Give the extent of all uninfected red blood cells.
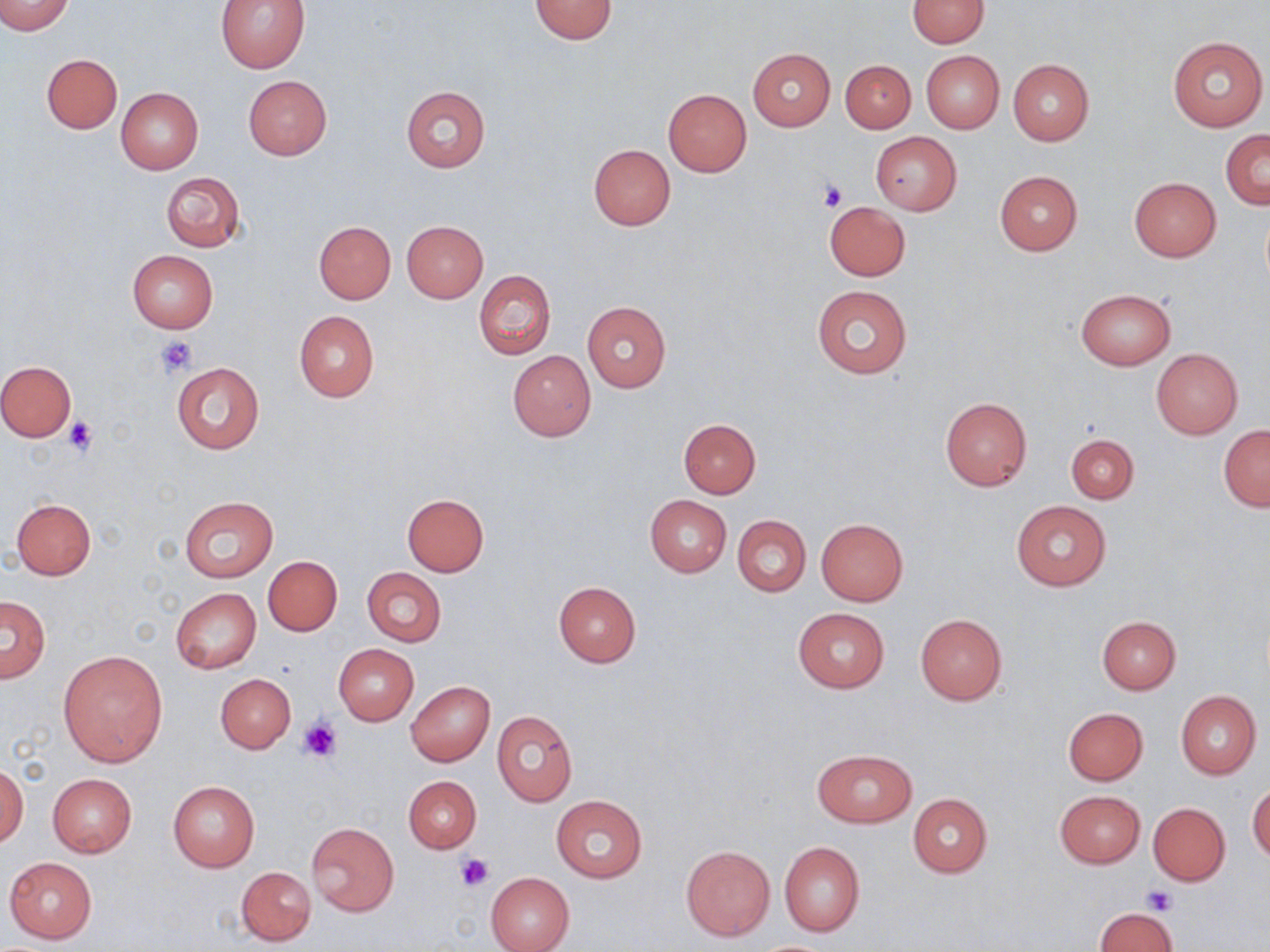
Approximate bounding boxes as (x1,y1)-(x2,y2) corner pairs in pixels.
Uninfected red blood cells: (0,0)-(73,35), (214,0)-(311,72), (529,0)-(617,43), (907,1)-(989,47), (1167,35)-(1267,131), (747,48)-(836,131), (921,51)-(1003,133), (42,53)-(122,134), (1007,58)-(1094,146), (841,60)-(915,132), (242,76)-(332,160), (401,86)-(490,171), (116,87)-(203,175), (663,88)-(751,176), (1221,129)-(1269,209), (872,133)-(962,214), (587,144)-(676,231), (161,171)-(244,252), (995,171)-(1082,256), (1128,177)-(1221,262), (825,202)-(911,281), (403,220)-(488,303), (313,221)-(395,303), (127,249)-(218,334), (474,270)-(555,358), (811,286)-(912,377), (1076,289)-(1176,369), (582,301)-(671,393), (294,309)-(379,403), (1151,349)-(1242,438), (508,350)-(596,441), (0,361)-(75,441), (171,362)-(265,454), (940,397)-(1032,490), (679,418)-(761,497), (1219,424)-(1270,511), (1066,433)-(1139,503), (402,493)-(490,576), (644,495)-(732,578), (180,497)-(278,581), (11,499)-(96,579), (1011,499)-(1111,591), (733,515)-(811,597), (815,518)-(908,606), (262,556)-(342,636), (361,567)-(446,647), (553,581)-(640,667), (170,588)-(262,674), (1,595)-(50,682), (793,608)-(890,692), (915,613)-(1007,705), (1098,616)-(1180,694), (333,644)-(419,726), (59,650)-(168,766), (215,674)-(295,753), (406,681)-(495,766), (1176,690)-(1261,778), (1064,707)-(1148,785), (492,711)-(577,806), (811,749)-(915,827), (1,763)-(28,847), (48,774)-(136,856), (403,776)-(481,852), (167,780)-(261,873), (1248,782)-(1270,864), (1054,790)-(1145,867), (908,793)-(993,877), (551,795)-(647,882), (1147,802)-(1230,885), (307,821)-(399,917), (779,841)-(865,937), (680,844)-(776,941), (5,856)-(97,944), (237,866)-(316,946), (485,872)-(575,952), (1095,907)-(1179,950).

slide-level diagnosis = negative for blood parasites
image size = 1270×952 pixels
magnification = 1000x
modality = light microscopy
preparation = thin blood smear
stain = May-Grünwald-Giemsa
field of view = single
platelet locations = approximate bounding boxes as (x1,y1)-(x2,y2) corner pairs in pixels: (819,180)-(849,211), (154,335)-(197,379), (65,416)-(97,458), (298,715)-(344,763), (455,853)-(494,890), (1141,884)-(1176,915)